Locate platelets.
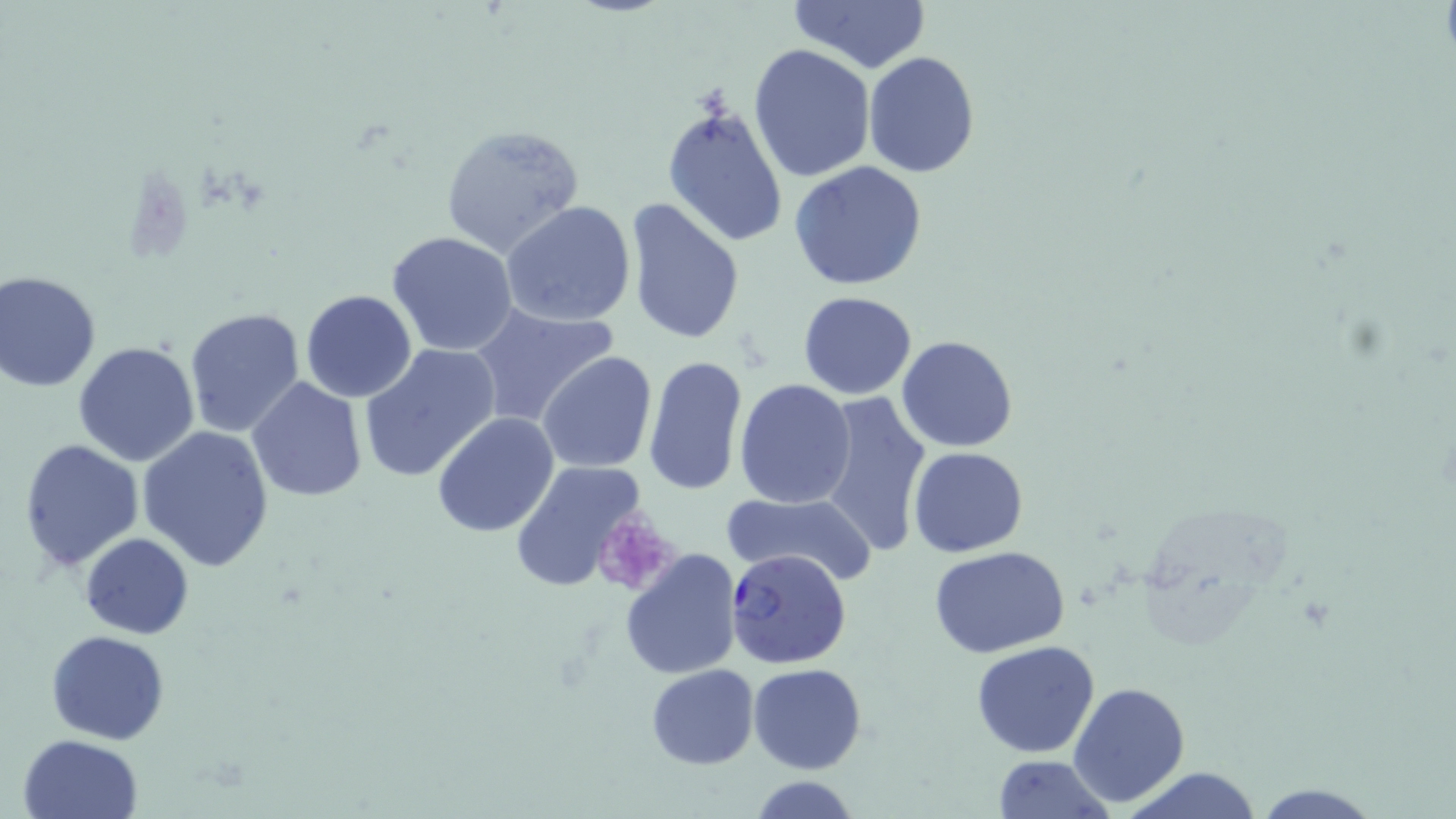
Approximate bounding boxes as (x1, y1, x2, y2) in pixels.
Platelets: (591, 515, 675, 596).

Uninfected red blood cell locations: (789, 0, 933, 74), (748, 43, 876, 182), (862, 51, 981, 177), (661, 100, 790, 248), (439, 123, 584, 258), (789, 161, 928, 290), (624, 198, 745, 345), (499, 200, 636, 327), (387, 231, 519, 357), (0, 273, 102, 392), (301, 290, 417, 402), (798, 291, 918, 400), (468, 302, 620, 430), (183, 306, 306, 437), (897, 335, 1020, 452), (73, 341, 200, 467), (358, 344, 502, 484), (537, 351, 659, 472), (642, 355, 748, 497), (245, 378, 369, 502), (734, 378, 855, 508), (813, 389, 934, 562), (432, 410, 560, 537), (138, 426, 274, 572), (18, 440, 145, 572), (908, 446, 1028, 557), (511, 461, 649, 596), (723, 489, 879, 586), (80, 532, 193, 640), (931, 547, 1071, 659), (620, 548, 743, 681), (46, 630, 170, 745), (971, 641, 1100, 757), (748, 662, 867, 774), (646, 665, 759, 769), (1067, 680, 1192, 809), (18, 734, 145, 819), (991, 755, 1117, 819), (1116, 767, 1265, 819), (747, 777, 861, 817). Plasmodium falciparum-infected red blood cell locations: (725, 547, 852, 668). Slide-level diagnosis: Plasmodium falciparum. Thin blood smear. Optical microscopy. May-Grünwald-Giemsa stain. Captured at 1000x magnification. Single field of view. Image is 1456×819 pixels.